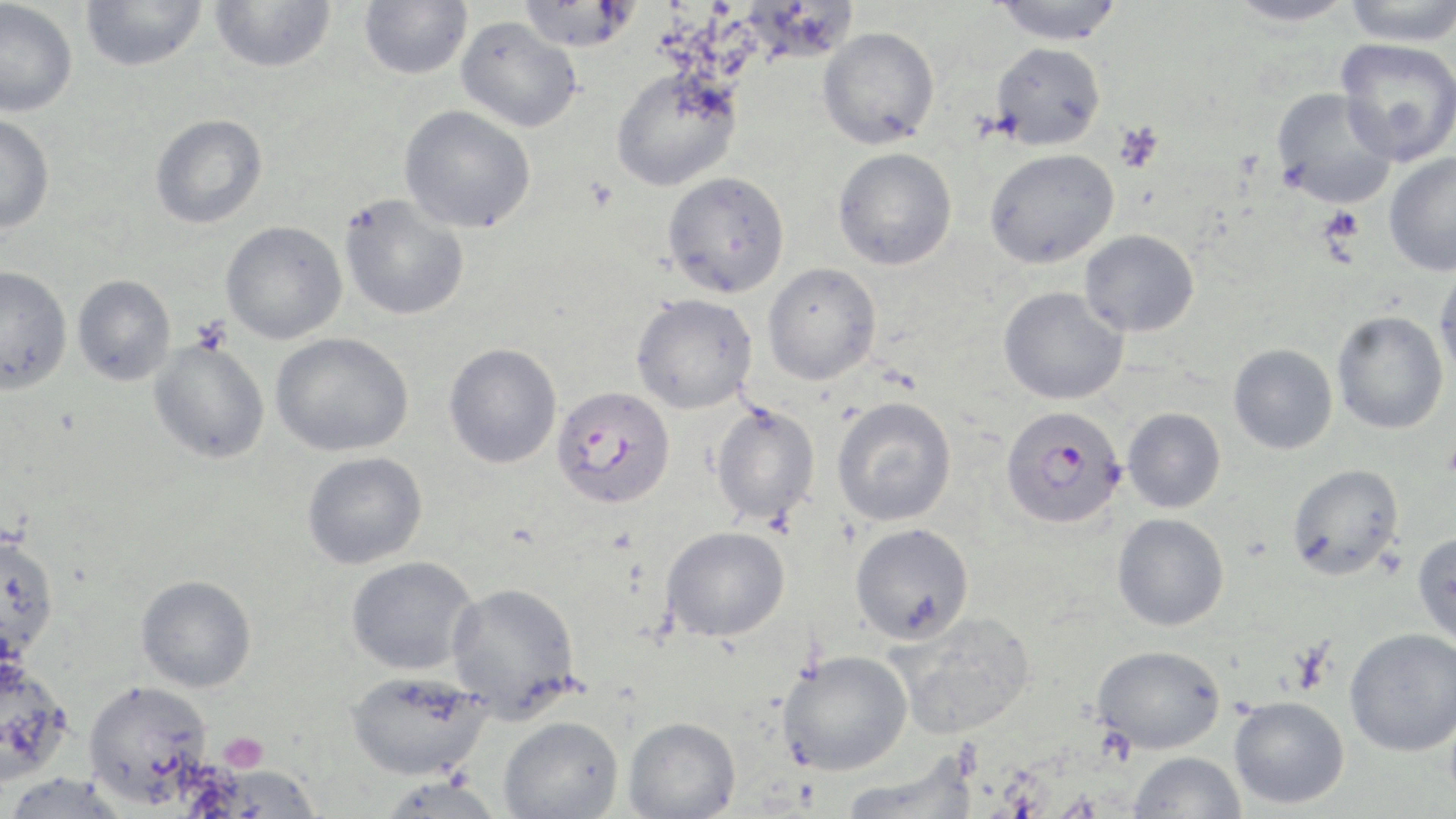

Summary:
  - Coordinate format: approximate bounding boxes as (x1,y1)-(x2,y2) corner pairs in pixels
  - Uninfected red blood cell locations: (80,0)-(207,72), (209,0)-(337,74), (358,0)-(473,79), (518,0)-(639,52), (991,0)-(1124,46), (1227,0)-(1358,27), (1343,0)-(1456,47), (0,1)-(78,117), (457,17)-(582,132), (817,26)-(940,149), (1335,38)-(1456,166), (990,42)-(1106,151), (610,65)-(743,191), (1272,87)-(1398,209), (399,105)-(537,233), (0,114)-(55,234), (149,114)-(267,229), (833,147)-(957,270), (984,148)-(1119,269), (1384,152)-(1456,276), (662,170)-(790,298), (339,194)-(470,321), (220,221)-(347,345), (1080,229)-(1199,337), (1433,261)-(1456,385), (763,262)-(881,385), (0,265)-(73,395), (72,274)-(176,385), (998,286)-(1129,405), (631,292)-(758,414), (1332,310)-(1449,435), (270,332)-(414,457), (148,339)-(271,464), (443,342)-(562,469), (1228,343)-(1338,454), (831,396)-(957,526), (709,402)-(821,526), (1122,407)-(1226,513), (302,451)-(428,569), (1286,463)-(1405,581), (1112,512)-(1230,631), (849,522)-(974,644), (661,526)-(790,642), (0,531)-(59,659), (1412,531)-(1456,645), (345,556)-(479,675), (135,574)-(257,693), (447,581)-(582,719), (887,611)-(1036,739), (1344,628)-(1456,756), (1092,644)-(1226,754), (777,649)-(913,776), (0,658)-(74,786), (346,670)-(491,781), (1229,696)-(1349,809), (498,716)-(624,819), (623,716)-(741,819), (1128,751)-(1247,819), (839,755)-(979,818), (194,764)-(322,817), (0,772)-(130,819), (375,775)-(503,819)
  - Plasmodium falciparum-infected red blood cell locations: (550,386)-(677,509), (997,409)-(1124,533), (83,680)-(213,806)
  - Platelet locations: (1113,120)-(1164,174), (1320,207)-(1365,247), (219,732)-(269,773)
  - Slide-level diagnosis: Plasmodium falciparum
  - Magnification: 1000x
  - Preparation: thin blood film
  - Modality: light microscopy
  - Stain: May-Grünwald-Giemsa
  - Field of view: one of a larger specimen
  - Image size: 1456×819 pixels